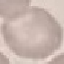
malaria_status: uninfected
stain: Giemsa
preparation: thin smear
capture: smartphone through the microscope eyepiece
image_type: automatically extracted cell patch, resized to 64 × 64 pixels